Report the malaria status of this cell.
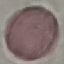

It is uninfected.

Thin blood smear. Giemsa stain. Photographed with a smartphone camera at the microscope eyepiece. Cell patch, automatically extracted from a larger field of view and resized to 64 × 64 pixels.